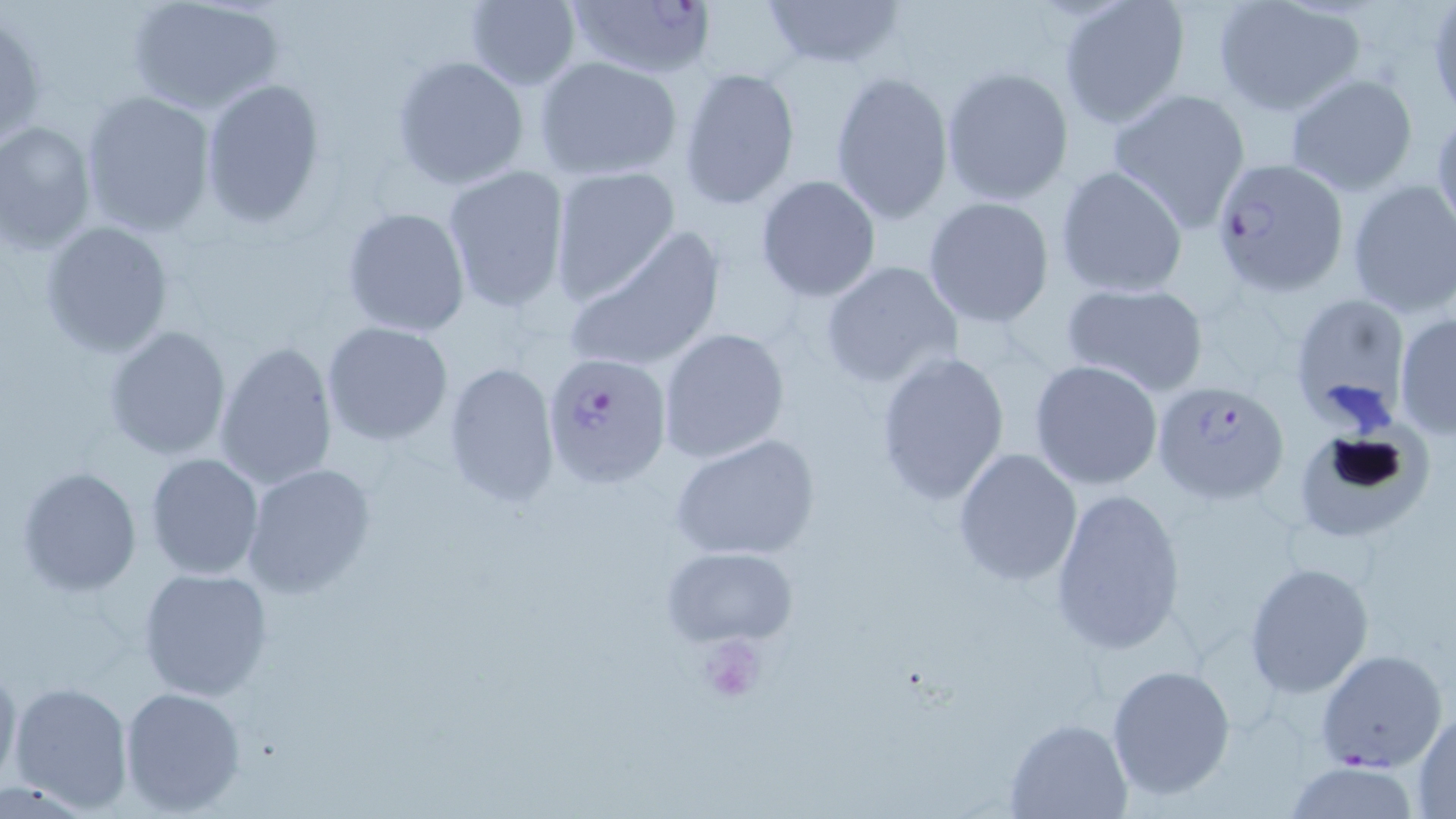

{
  "slide_level_diagnosis": "Plasmodium falciparum",
  "magnification": "1000x",
  "stain": "May-Grünwald-Giemsa",
  "uninfected_red_blood_cell_locations": "approximate bounding boxes as [x1, y1, x2, y2] in pixels: [124, 0, 285, 115], [756, 0, 911, 70], [462, 1, 582, 90], [1056, 1, 1190, 129], [1213, 1, 1364, 117], [1, 12, 46, 153], [391, 54, 530, 191], [534, 55, 683, 182], [678, 66, 801, 210], [940, 66, 1072, 206], [829, 68, 954, 227], [1283, 73, 1420, 196], [198, 79, 327, 228], [1106, 88, 1252, 234], [80, 91, 217, 236], [1430, 105, 1456, 242], [0, 122, 97, 254], [441, 164, 570, 313], [1055, 165, 1189, 298], [548, 167, 680, 306], [755, 174, 882, 303], [1346, 179, 1456, 317], [922, 196, 1056, 327], [341, 205, 471, 337], [39, 220, 174, 359], [563, 228, 728, 375], [820, 261, 964, 391], [1059, 280, 1211, 397], [1286, 291, 1411, 428], [1394, 311, 1456, 440], [322, 321, 454, 446], [103, 325, 232, 462], [656, 327, 790, 465], [215, 341, 339, 490], [873, 349, 1011, 506], [440, 360, 560, 509], [1029, 360, 1164, 489], [1291, 423, 1433, 545], [670, 433, 821, 562], [952, 448, 1083, 583], [144, 452, 265, 580], [242, 463, 378, 597], [15, 465, 143, 595], [1048, 486, 1188, 656], [661, 545, 798, 647], [1242, 560, 1375, 699], [137, 566, 274, 700], [1315, 649, 1448, 772], [0, 655, 21, 793], [1105, 663, 1237, 802], [8, 680, 133, 814], [119, 685, 247, 816], [1411, 707, 1456, 814], [1006, 717, 1131, 818], [1279, 760, 1426, 817]",
  "preparation": "thin blood smear",
  "modality": "optical microscopy",
  "field_of_view": "single",
  "platelet_locations": "approximate bounding boxes as [x1, y1, x2, y2] in pixels: [693, 633, 768, 706]",
  "plasmodium_falciparum_infected_red_blood_cell_locations": "approximate bounding boxes as [x1, y1, x2, y2] in pixels: [565, 0, 719, 83], [1211, 156, 1350, 296], [544, 354, 674, 490], [1148, 379, 1285, 501]",
  "image_size": "1456×819 pixels"
}